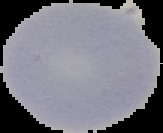
image type = segmented cell region on a black background
malaria status = uninfected
preparation = thin blood film
image size = 163×133 pixels